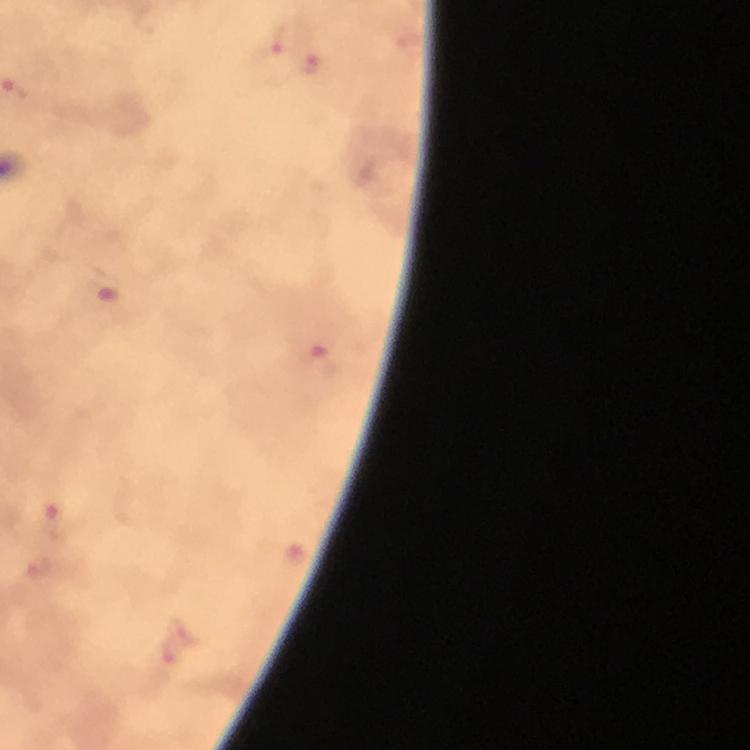

preparation: thick smear
plasmodium_parasite_locations: 'approximate centers as {x, y} in pixels: {270, 50}, {314, 64}, {319, 360}, {57, 523}'
capture: smartphone mounted on the microscope
image_size: 750×750 pixels
magnification: 100x
context: from a malaria diagnostic workup
immersion_oil: used
cropped_from: one field of view
stain: Giemsa